Assess this cell for malaria.
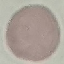

Uninfected.

Cell patch, automatically extracted from a larger field of view and resized to 64 × 64 pixels. Giemsa stain. Thin blood smear. Photographed with a smartphone camera at the microscope eyepiece.